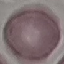

Malaria status: uninfected. Automatically extracted cell patch, resized to 64 × 64 pixels. Thin blood smear. Acquired by smartphone through the microscope eyepiece. Giemsa stain.